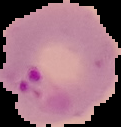

image size = 121×127 pixels
image type = segmented cell region with the area outside set to black
preparation = thin blood smear
malaria status = parasitized